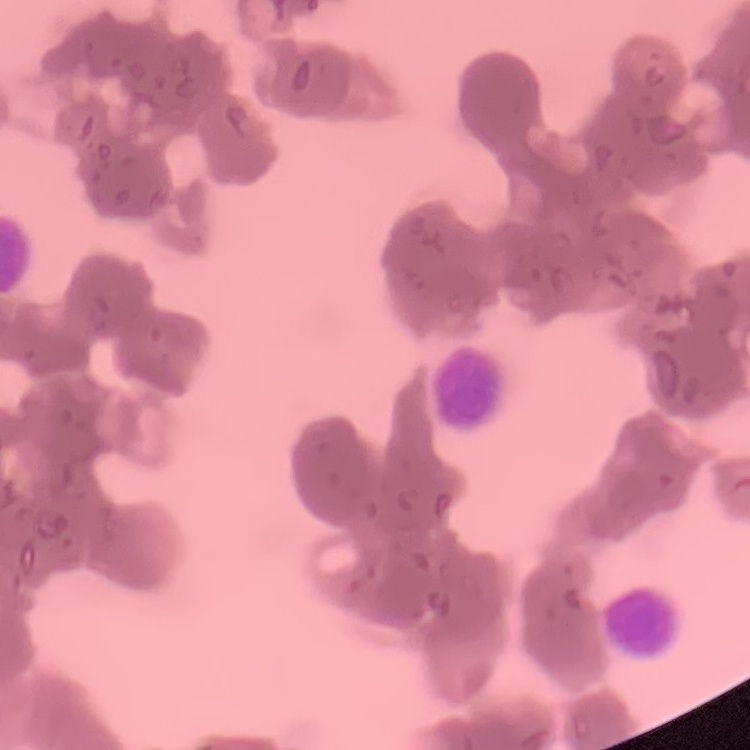 The red blood cells show rouleaux formation. One tile cut from a larger photomicrograph. Thin peripheral smear. Stained with either Field's or Giemsa.